Locate every blood parasite and identify its species.
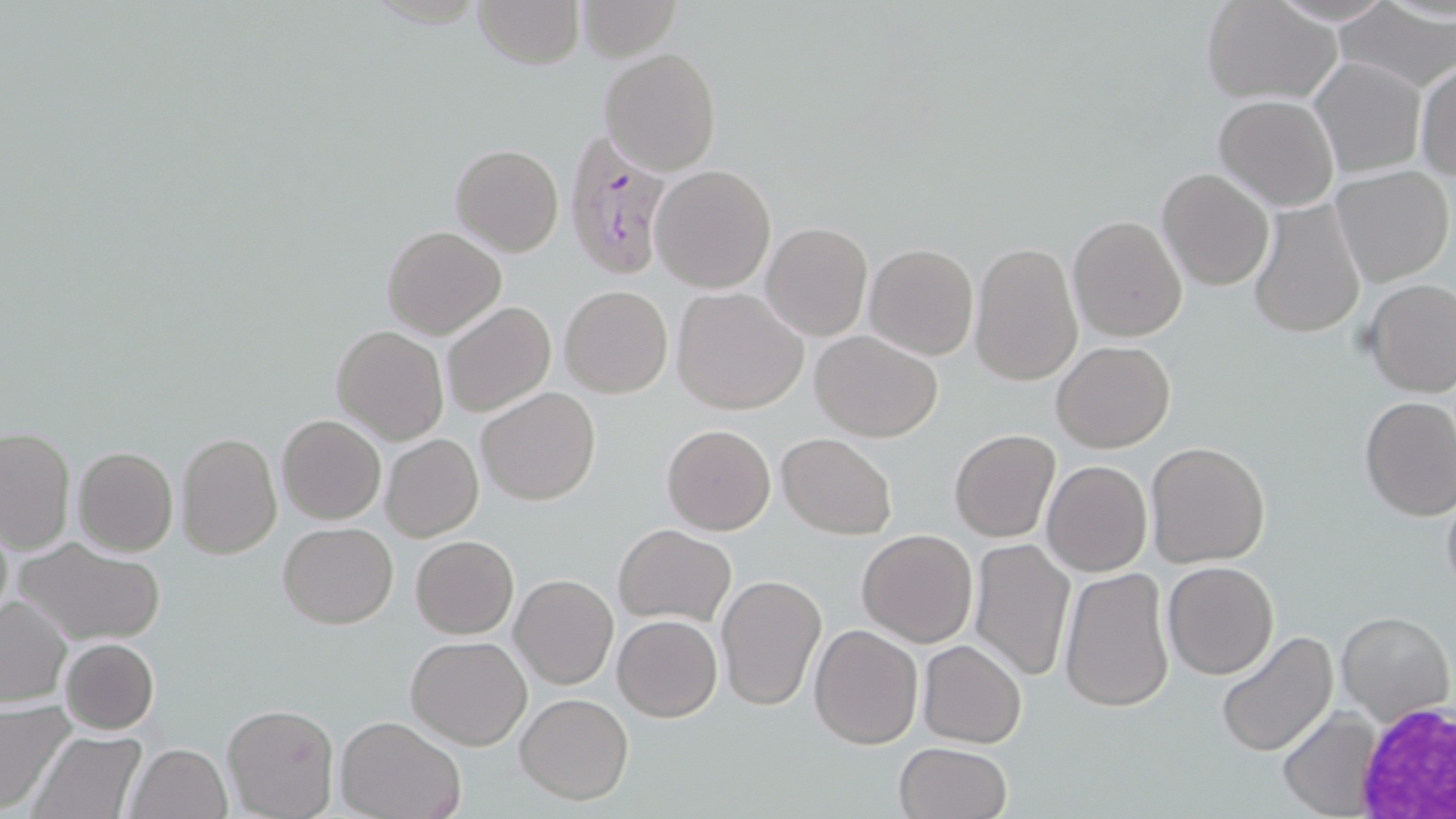
Approximate bounding boxes as (x1, y1, x2, y2) in pixels.
Plasmodium falciparum-infected red blood cells: (563, 129, 677, 280).
No Plasmodium ovale, Plasmodium malariae, Plasmodium vivax, Babesia divergens, or Trypanosoma brucei observed.

slide-level diagnosis = Plasmodium falciparum
magnification = 1000x
preparation = thin blood film
stain = May-Grünwald-Giemsa
white blood cell locations = approximate bounding boxes as (x1, y1, x2, y2) in pixels: (1354, 697, 1456, 814)
uninfected red blood cell locations = approximate bounding boxes as (x1, y1, x2, y2) in pixels: (473, 0, 585, 69), (576, 1, 682, 62), (1199, 1, 1347, 105), (1334, 3, 1455, 93), (599, 47, 722, 176), (1311, 58, 1427, 178), (1414, 61, 1456, 184), (1214, 94, 1339, 211), (450, 143, 563, 257), (650, 164, 776, 293), (1331, 165, 1455, 287), (1157, 168, 1275, 291), (1247, 197, 1367, 340), (1067, 215, 1187, 341), (761, 222, 873, 341), (381, 225, 507, 340), (969, 241, 1084, 386), (864, 243, 979, 361), (1363, 279, 1456, 398), (559, 283, 673, 398), (674, 288, 808, 413), (442, 301, 556, 419), (332, 325, 449, 443), (811, 330, 945, 442), (1052, 340, 1175, 452), (477, 387, 602, 506), (1358, 394, 1456, 520), (278, 414, 386, 525), (662, 423, 777, 535), (0, 426, 75, 554), (949, 429, 1061, 542), (176, 431, 281, 559), (381, 432, 485, 542), (776, 432, 898, 540), (1145, 442, 1270, 568), (73, 446, 178, 556), (1042, 460, 1152, 578), (1440, 478, 1456, 602), (278, 522, 398, 628), (614, 524, 736, 627), (857, 529, 980, 647), (410, 536, 518, 638), (968, 536, 1077, 682), (12, 538, 166, 646), (1163, 562, 1280, 680), (1060, 566, 1174, 712), (716, 573, 826, 712), (511, 574, 618, 689), (0, 596, 72, 708), (1335, 611, 1453, 725), (614, 614, 722, 721), (810, 624, 924, 749), (1213, 628, 1339, 757), (406, 636, 532, 750), (59, 637, 159, 734), (918, 640, 1027, 748), (515, 692, 634, 805), (0, 703, 75, 814), (222, 703, 340, 819), (1279, 707, 1385, 818), (336, 715, 467, 819), (27, 729, 147, 818), (894, 741, 1014, 819), (126, 743, 231, 819)
field of view = single
modality = light microscopy
image size = 1456×819 pixels